Classify this cell by malaria status.
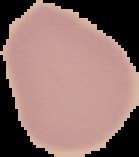
It is uninfected.

From a thin blood film. Cell region segmented out of the field of view; the surrounding area is masked to black. Image is 139×157 pixels.